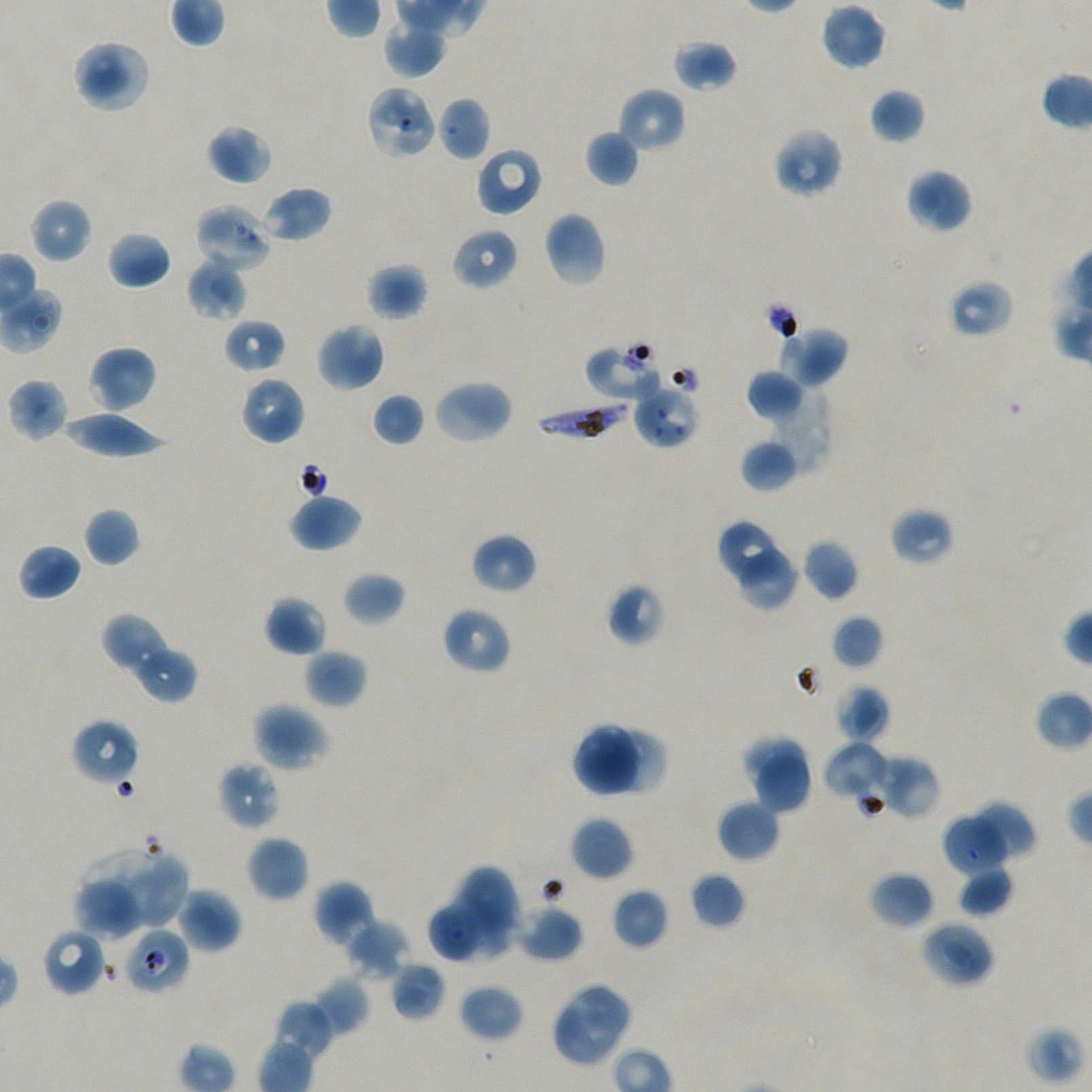

Approximate bounding boxes as {x1, y1, x2, y2} in pixels. Not every red blood cell is marked.
Summary:
  - Locations of red blood cells of indeterminate infection status: {369, 88, 435, 157}, {195, 204, 272, 273}, {585, 341, 663, 401}, {633, 389, 702, 446}, {123, 928, 189, 996}
  - Locations of infected red blood cells: {536, 399, 632, 441}
  - Locations of uninfected red blood cells: {820, 3, 887, 71}, {382, 22, 446, 79}, {672, 38, 739, 93}, {72, 39, 151, 113}, {617, 88, 686, 153}, {869, 88, 926, 144}, {437, 96, 490, 162}, {206, 124, 272, 185}, {773, 127, 843, 198}, {585, 130, 640, 187}, {475, 147, 543, 217}, {905, 168, 972, 234}, {258, 186, 333, 243}, {29, 198, 92, 263}, {543, 211, 606, 287}, {451, 228, 519, 291}, {107, 230, 172, 290}, {186, 258, 248, 322}, {365, 263, 428, 321}, {953, 280, 1013, 334}, {223, 318, 287, 374}, {315, 323, 385, 392}, {780, 326, 849, 387}, {88, 345, 157, 414}, {746, 369, 806, 422}, {240, 376, 306, 445}, {7, 378, 69, 441}, {432, 378, 513, 445}, {756, 382, 831, 473}, {371, 393, 424, 447}, {59, 410, 169, 459}, {740, 439, 798, 492}, {289, 494, 363, 552}, {84, 507, 140, 566}, {888, 507, 956, 566}, {721, 522, 776, 583}, {470, 532, 537, 595}, {802, 539, 859, 601}, {18, 543, 82, 601}, {740, 546, 798, 609}, {342, 571, 405, 626}, {606, 582, 666, 647}, {264, 596, 327, 656}, {441, 606, 511, 674}, {831, 614, 883, 670}, {101, 616, 161, 666}, {117, 630, 168, 678}, {304, 649, 367, 709}, {138, 651, 198, 704}, {836, 683, 889, 743}, {252, 703, 331, 771}, {71, 718, 139, 786}, {572, 725, 644, 799}, {604, 730, 666, 794}, {742, 733, 806, 788}, {825, 743, 886, 794}, {755, 754, 810, 810}, {879, 754, 941, 819}, {218, 761, 281, 831}, {716, 799, 780, 862}, {971, 802, 1036, 860}, {570, 816, 634, 881}, {946, 818, 1008, 876}, {246, 835, 310, 903}, {86, 845, 170, 928}, {133, 856, 189, 930}, {460, 866, 516, 928}, {958, 867, 1013, 915}, {869, 871, 934, 930}, {689, 872, 746, 929}, {314, 880, 376, 946}, {74, 881, 143, 939}, {447, 887, 520, 958}, {177, 888, 242, 953}, {612, 888, 669, 950}, {427, 900, 480, 962}, {515, 904, 583, 963}, {344, 919, 410, 980}, {920, 920, 996, 987}, {41, 928, 107, 997}, {390, 961, 445, 1021}, {312, 976, 369, 1036}, {458, 984, 524, 1042}, {569, 986, 630, 1045}, {273, 999, 335, 1060}, {556, 1000, 616, 1064}
  - Culture: P. falciparum strain NF54, static, in vitro
  - Donor blood group: A+/O+
  - Image size: 1092×1092 pixels
  - Objective: 100x, oil immersion, numerical aperture 1.45
  - Preparation: thin blood film
  - Stain: Giemsa
  - Field of view: single